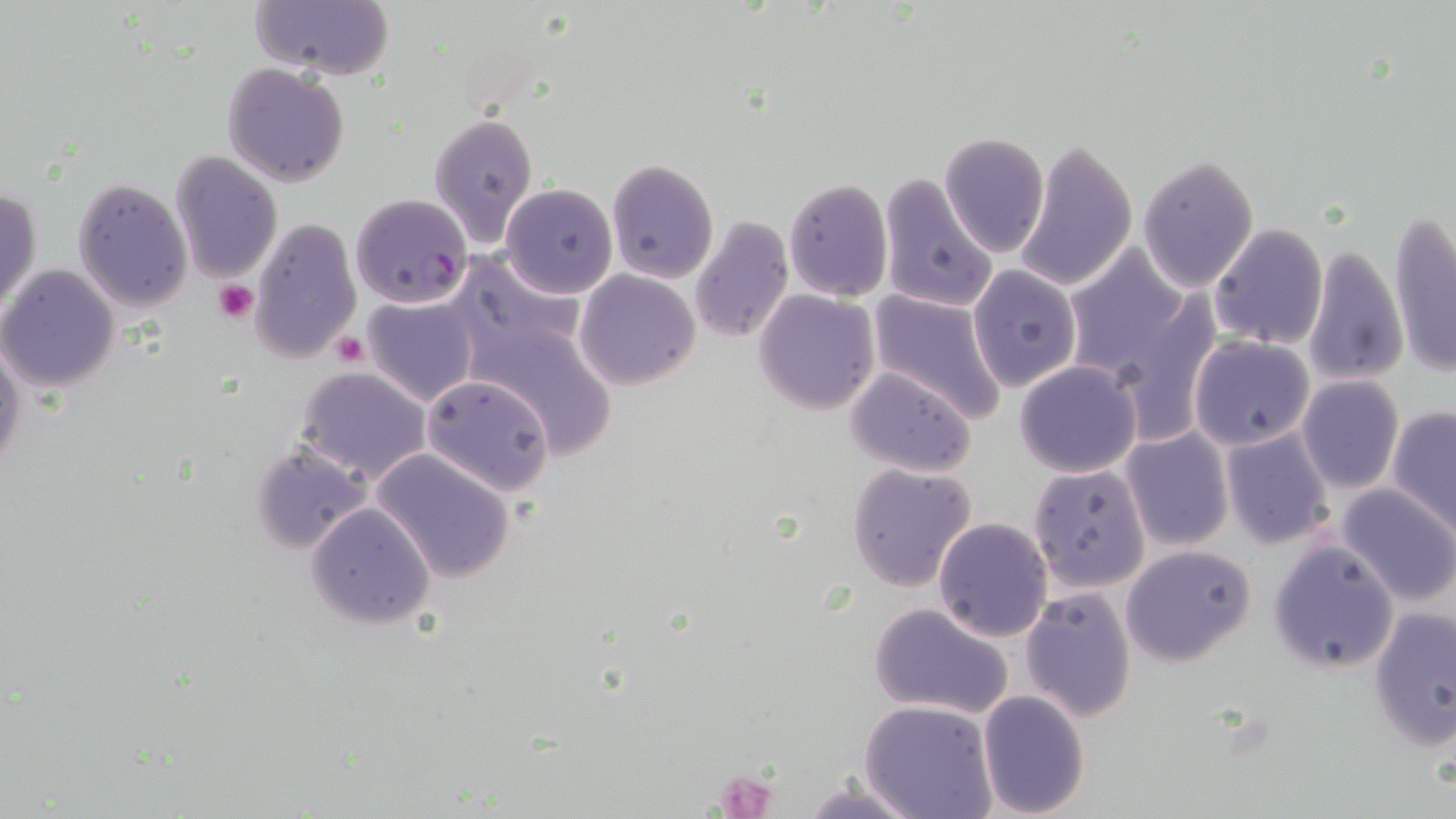 Approximate bounding boxes as (x1,y1)-(x2,y2) corner pairs in pixels. Uninfected red blood cell locations: (249,0)-(395,82), (221,62)-(351,187), (427,113)-(539,244), (938,132)-(1050,258), (1017,139)-(1138,293), (170,149)-(282,284), (1135,153)-(1260,292), (607,159)-(719,282), (879,174)-(997,315), (71,177)-(194,312), (784,178)-(893,301), (500,182)-(616,299), (1,186)-(41,317), (1388,211)-(1456,376), (249,216)-(362,365), (688,217)-(794,342), (1209,223)-(1327,350), (1300,243)-(1409,387), (1063,244)-(1196,381), (452,253)-(587,360), (967,263)-(1083,393), (0,264)-(121,395), (574,269)-(701,390), (866,289)-(1007,422), (753,290)-(880,414), (362,294)-(480,406), (467,309)-(621,457), (0,333)-(25,481), (1188,335)-(1315,451), (1013,360)-(1143,477), (844,365)-(978,478), (295,366)-(432,483), (421,374)-(555,494), (1296,375)-(1405,494), (1387,406)-(1456,535), (1219,427)-(1336,552), (1120,428)-(1233,552), (251,441)-(370,554), (1029,441)-(1233,570), (372,448)-(518,583), (846,462)-(978,593), (1026,462)-(1151,594), (1337,482)-(1456,606), (305,503)-(436,631), (933,517)-(1052,640), (1268,539)-(1398,672), (1120,544)-(1256,665), (1020,588)-(1138,721), (868,600)-(1015,719), (1367,603)-(1455,751), (976,689)-(1092,816), (859,698)-(1000,819), (798,779)-(925,818). Plasmodium falciparum-infected red blood cell locations: (349,193)-(473,309). Platelet locations: (213,278)-(260,324), (331,332)-(368,366), (714,766)-(781,819). Slide-level diagnosis: Plasmodium falciparum. Thin blood smear. May-Grünwald-Giemsa-stained preparation. Image is 1456×819 pixels. Optical microscopy. 1000x magnification. Single field of view.